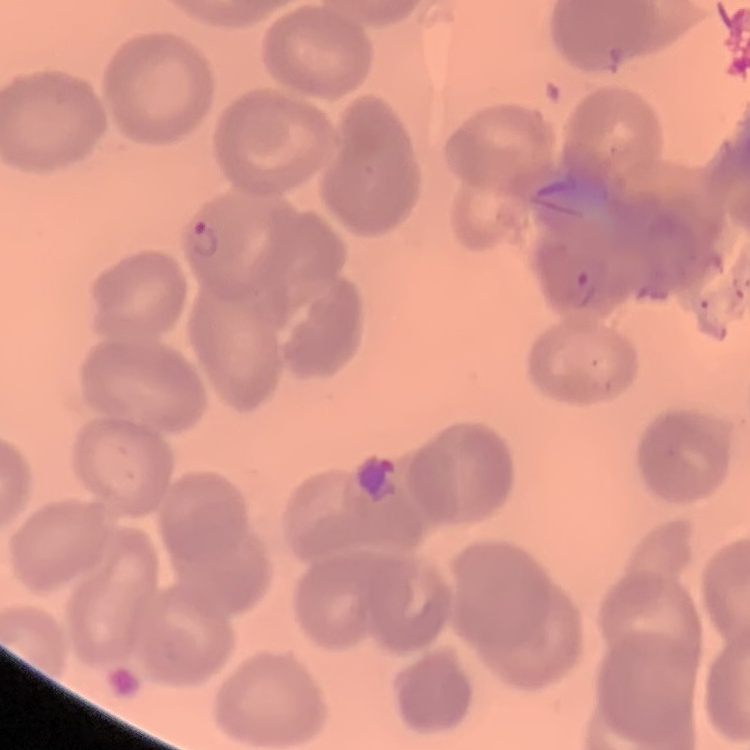
erythrocyte morphology = no rouleaux formation
preparation = thin peripheral smear
stain = Field's or Giemsa
image type = square crop of a larger photomicrograph